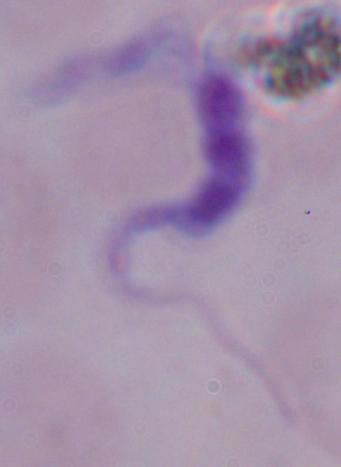

Summary:
  - Magnification: 1000x
  - Identification: trypanosome
  - Modality: micrograph